Report the malaria status of this cell.
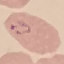

Parasitized.

Summary:
  - Capture: smartphone camera at the microscope eyepiece
  - Stain: Giemsa
  - Preparation: thin smear
  - Image type: automatically extracted cell patch, resized to 64 × 64 pixels